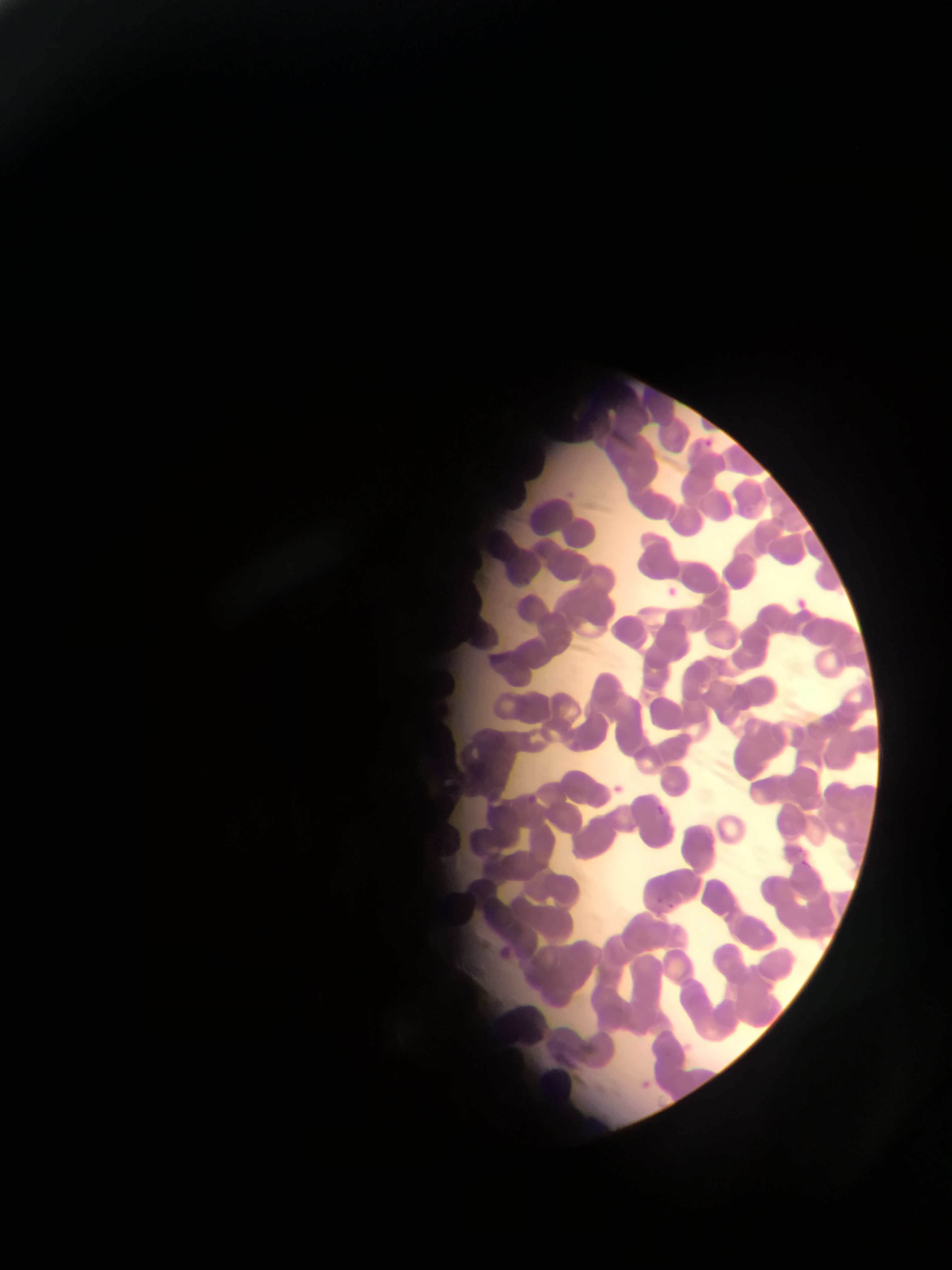 Approximate bounding boxes as (left, top, right, bottom) in pixels. Plasmodium parasite locations: (654, 801, 666, 815), (801, 857, 813, 869). Image is 952×1270 pixels. Collected in Ghana. Photographed through a microscope with a mobile-phone camera. One field of view. Thin blood film.